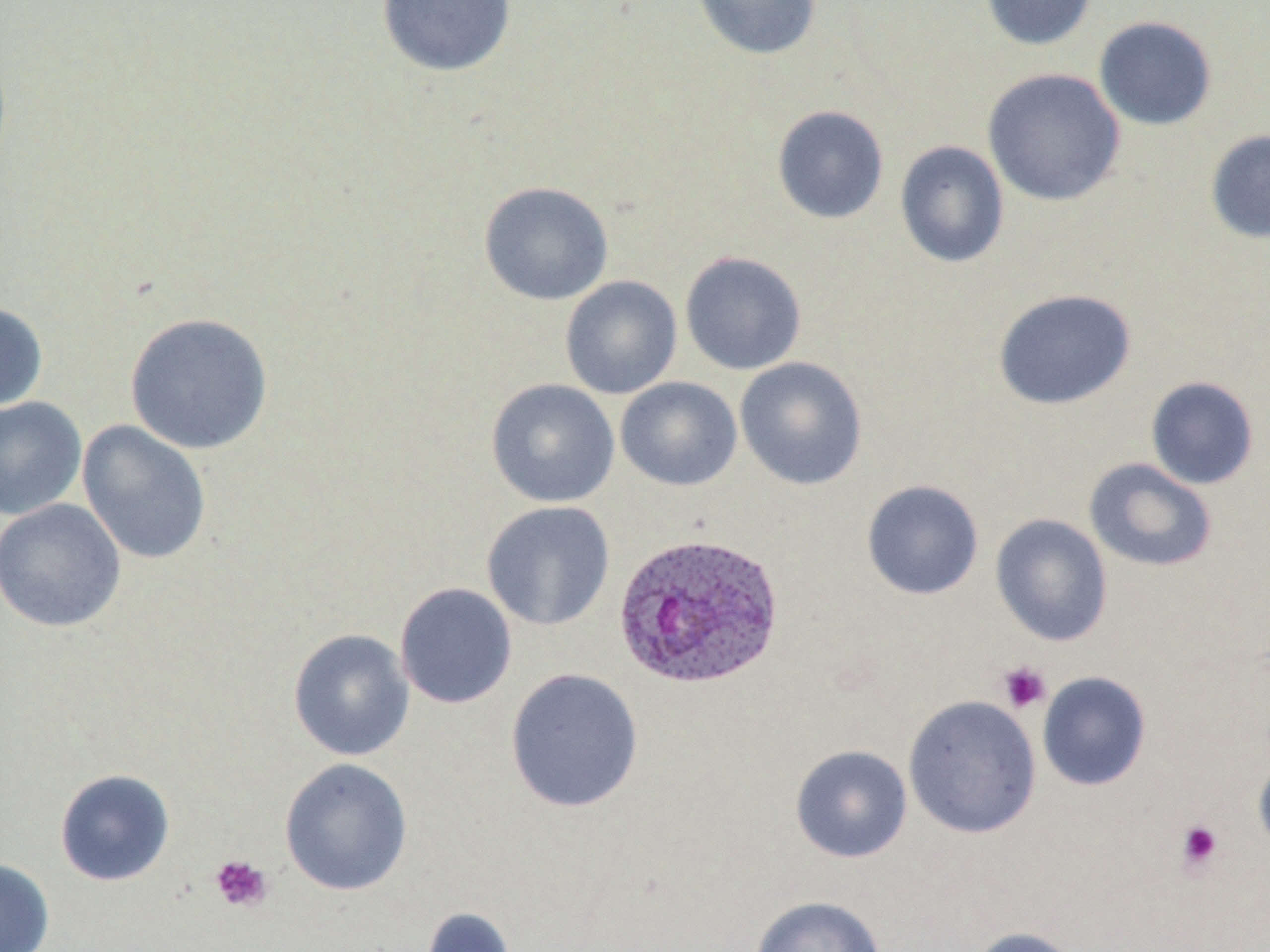
{
  "slide_level_diagnosis": "Plasmodium ovale",
  "platelet_locations": "approximate bounding boxes as [x1, y1, x2, y2] in pixels: [997, 661, 1052, 713], [1175, 819, 1224, 872], [210, 854, 273, 913]",
  "magnification": "1000x",
  "preparation": "thin blood film",
  "image_size": "1270×952 pixels",
  "field_of_view": "one of a larger specimen",
  "uninfected_red_blood_cell_locations": "approximate bounding boxes as [x1, y1, x2, y2] in pixels: [376, 0, 517, 78], [691, 0, 823, 60], [980, 0, 1097, 51], [1093, 16, 1218, 131], [982, 68, 1126, 207], [771, 105, 889, 224], [1205, 130, 1270, 244], [894, 140, 1010, 268], [478, 181, 614, 305], [680, 251, 807, 375], [560, 275, 682, 399], [992, 288, 1137, 410], [0, 299, 49, 413], [125, 312, 274, 455], [734, 357, 868, 490], [1145, 376, 1259, 489], [615, 377, 742, 491], [486, 378, 620, 508], [0, 396, 87, 521], [77, 420, 212, 566], [1083, 457, 1218, 573], [861, 479, 984, 600], [0, 498, 126, 632], [481, 501, 616, 631], [990, 513, 1113, 647], [394, 582, 518, 709], [288, 628, 415, 761], [504, 668, 644, 814], [1037, 671, 1152, 791], [903, 695, 1041, 839], [790, 745, 913, 863], [1253, 750, 1270, 859], [279, 757, 413, 896], [54, 768, 175, 887], [0, 857, 54, 952], [749, 895, 887, 952], [419, 906, 519, 952], [969, 926, 1084, 952]",
  "plasmodium_ovale_infected_red_blood_cell_locations": "approximate bounding boxes as [x1, y1, x2, y2] in pixels: [613, 531, 784, 690]",
  "stain": "May-Grünwald-Giemsa",
  "modality": "optical microscopy"
}